Assess for Plasmodium parasites.
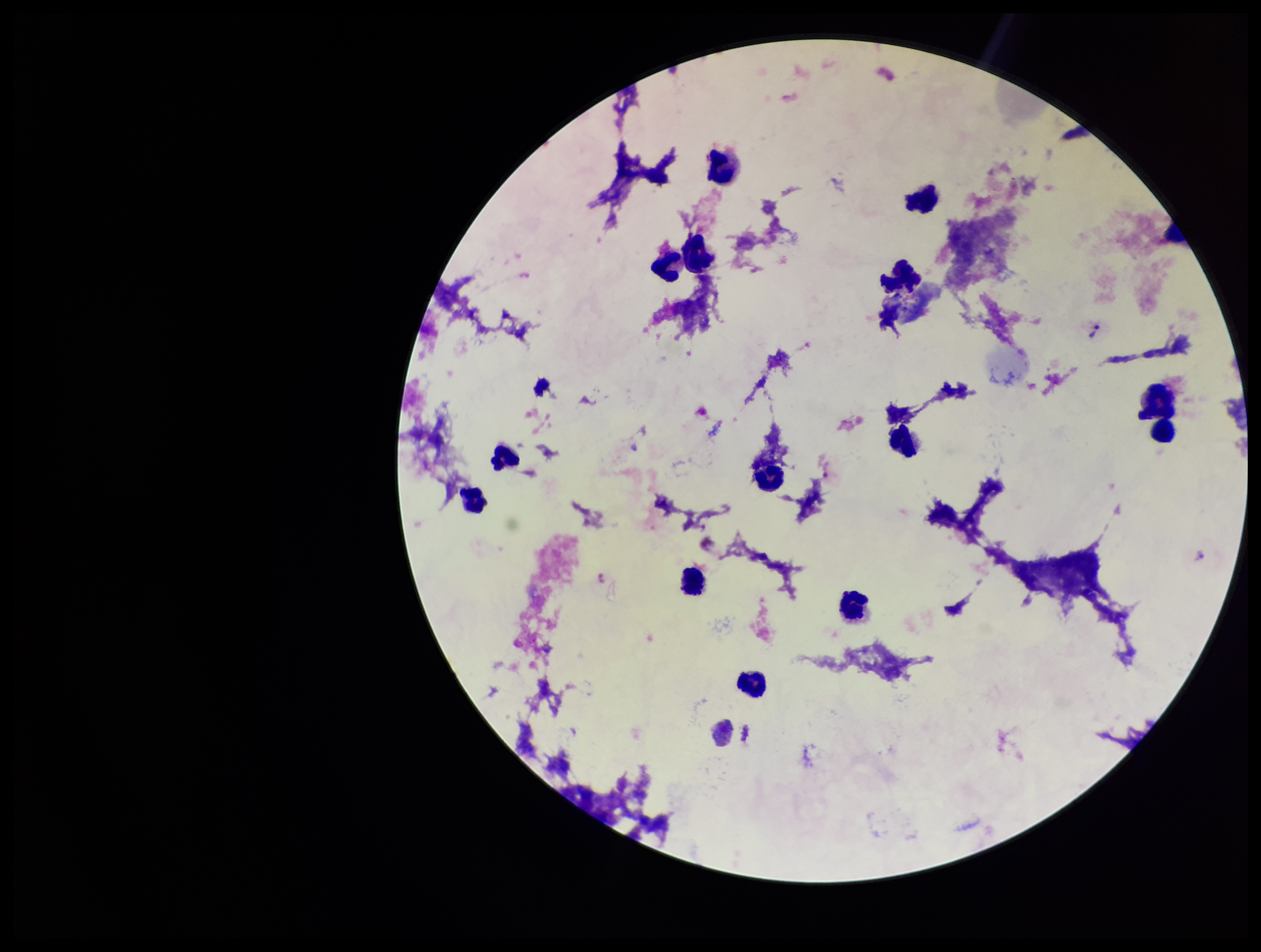
Detected.

Summary:
  - Species reported for this patient: Plasmodium vivax
  - Leukocyte count: 15
  - Preparation: thick blood smear
  - Parasite count: 3
  - Patient malaria status: positive
  - Stain: Giemsa
  - Capture: smartphone photograph through the microscope eyepiece
  - Image size: 1261×952 pixels
  - Field of view: single